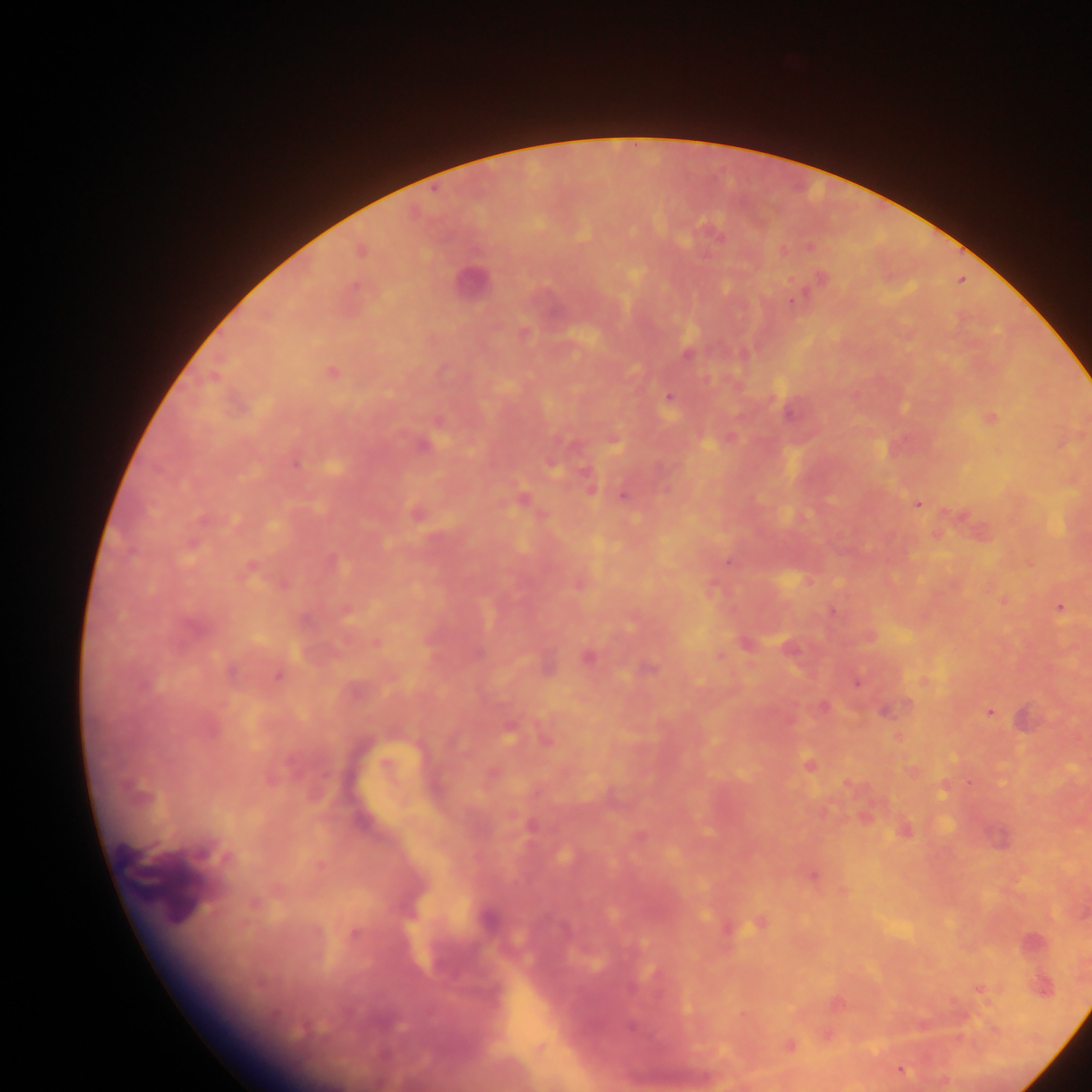

Approximate centers as [x, y] in pixels.
Summary:
  - Leukocyte locations: [469, 283]
  - Malaria parasite locations: [809, 247], [361, 251], [822, 278], [794, 301], [687, 354], [331, 372], [670, 398], [788, 414], [991, 418], [425, 446], [295, 464], [550, 465], [590, 488], [623, 497], [522, 500], [917, 505], [416, 513], [727, 562], [249, 569], [1060, 608], [346, 611], [833, 612], [193, 627], [377, 643], [747, 644], [789, 647], [719, 655], [587, 657], [648, 669], [231, 673], [278, 676], [857, 682], [822, 706], [887, 711], [990, 712], [509, 732], [545, 740], [808, 765], [204, 852], [813, 876], [254, 903], [759, 923], [354, 933], [980, 990], [630, 1026], [789, 1045], [902, 1070]
  - Country: Ghana
  - Image size: 1092×1092 pixels
  - Capture: mobile-phone photograph through a microscope
  - Preparation: thick blood smear
  - Field of view: single